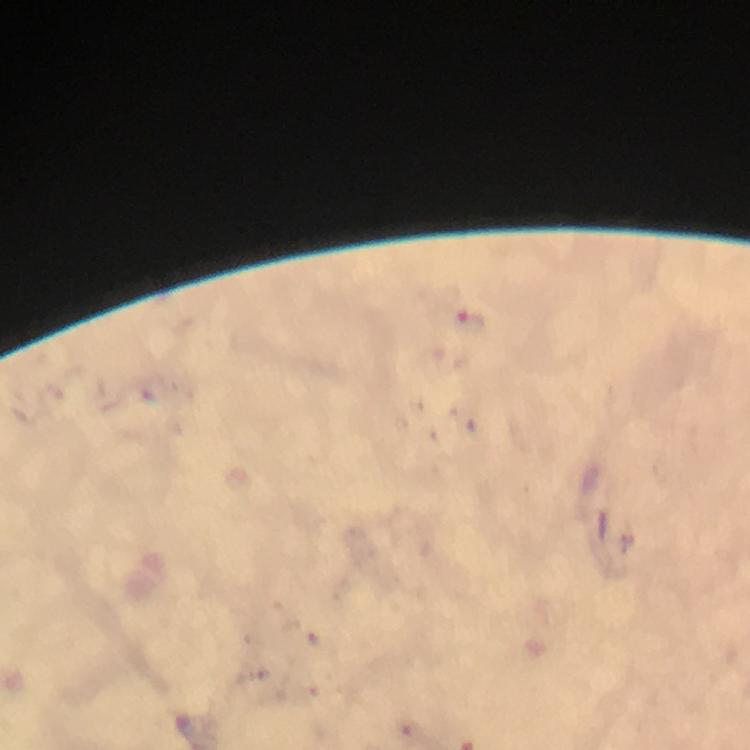

preparation: thick blood film
capture: smartphone mounted on the microscope
cropped_from: a single field of view
stain: Giemsa
magnification: 100x
image_size: 750×750 pixels
malaria_parasite_locations: 'approximate centers as (x, y) in pixels: (470, 321)'
context: from a diagnostic examination for malaria
immersion_oil: used